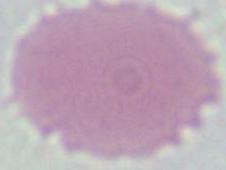

An erythrocyte is shown. Micrograph. 1000x magnification.